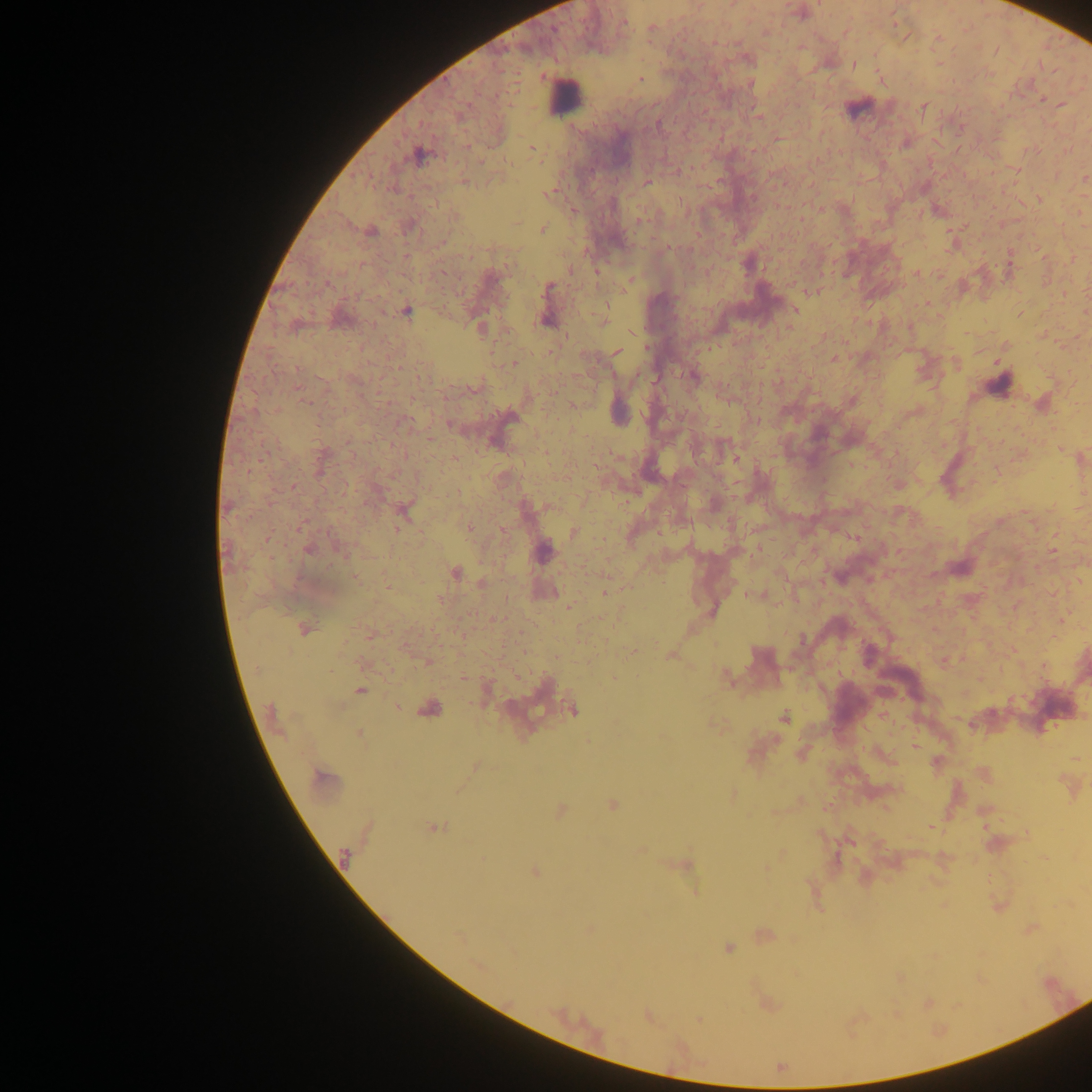

Approximate centers as {x, y} in pixels. Leukocyte locations: {564, 96}, {857, 108}, {999, 381}. Plasmodium parasite locations: {819, 4}, {623, 22}, {651, 31}, {854, 65}, {640, 80}, {1041, 99}, {1062, 105}, {924, 108}, {758, 116}, {658, 125}, {531, 148}, {418, 154}, {1085, 178}, {464, 182}, {647, 182}, {549, 193}, {1039, 199}, {639, 221}, {542, 230}, {370, 232}, {748, 265}, {596, 272}, {915, 273}, {631, 280}, {549, 287}, {814, 291}, {925, 305}, {795, 310}, {406, 311}, {603, 319}, {545, 320}, {481, 329}, {617, 352}, {835, 358}, {514, 362}, {694, 377}, {304, 401}, {736, 459}, {293, 486}, {404, 513}, {468, 527}, {574, 533}, {267, 538}, {309, 549}, {544, 550}, {455, 574}, {356, 579}, {605, 593}, {755, 595}, {441, 600}, {569, 607}, {1061, 620}, {303, 630}, {801, 640}, {631, 652}, {671, 656}, {427, 661}, {727, 677}, {360, 691}, {429, 709}, {573, 711}, {784, 717}, {359, 733}, {475, 766}, {323, 778}, {734, 794}, {613, 805}, {561, 810}, {434, 828}, {344, 855}, {536, 872}, {696, 891}, {728, 948}, {699, 1019}. Photographed through a microscope with a mobile-phone camera. Image is 1092×1092 pixels. Thick blood film. One field of view. Collected in Ghana.